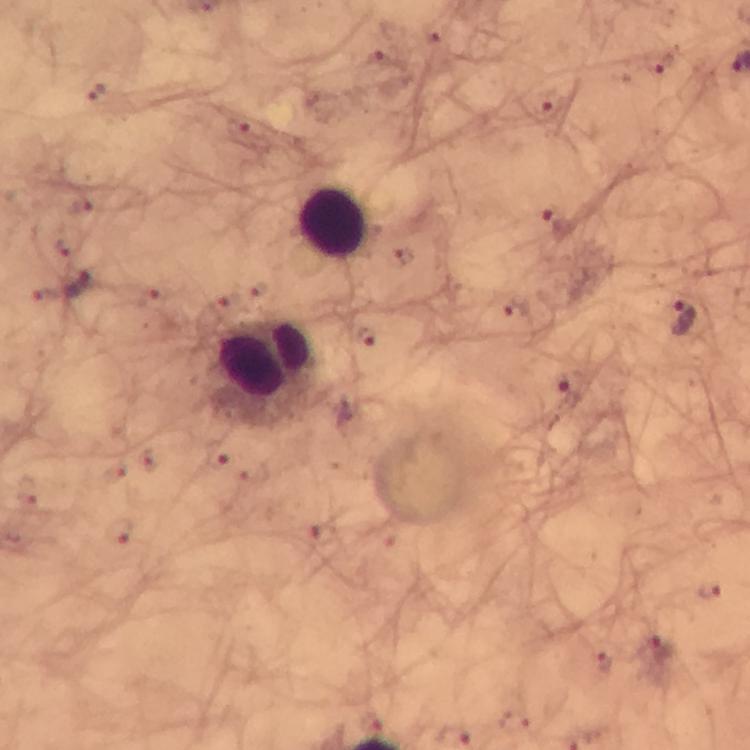 Approximate object centers, in pixels from the top-left corner. Plasmodium parasite locations: (x=379, y=57), (x=657, y=61), (x=96, y=92), (x=548, y=105), (x=558, y=226), (x=78, y=286), (x=685, y=318), (x=369, y=339), (x=573, y=383), (x=217, y=456), (x=116, y=529), (x=326, y=535), (x=707, y=590), (x=661, y=649), (x=603, y=661), (x=372, y=721). Leukocyte locations: (x=333, y=224), (x=268, y=369). Smartphone photograph taken through a microscope. From a malaria diagnostic workup. Image is 750×750 pixels. 100x magnification. Cropped region of a single field of view. Thick smear. Immersion oil applied. Giemsa-stained preparation.